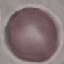
Result: no malaria parasites detected. Photographed with a smartphone camera at the microscope eyepiece. Thin blood smear. Cell patch, automatically extracted from a larger field of view and resized to 64 × 64 pixels. Giemsa stain.